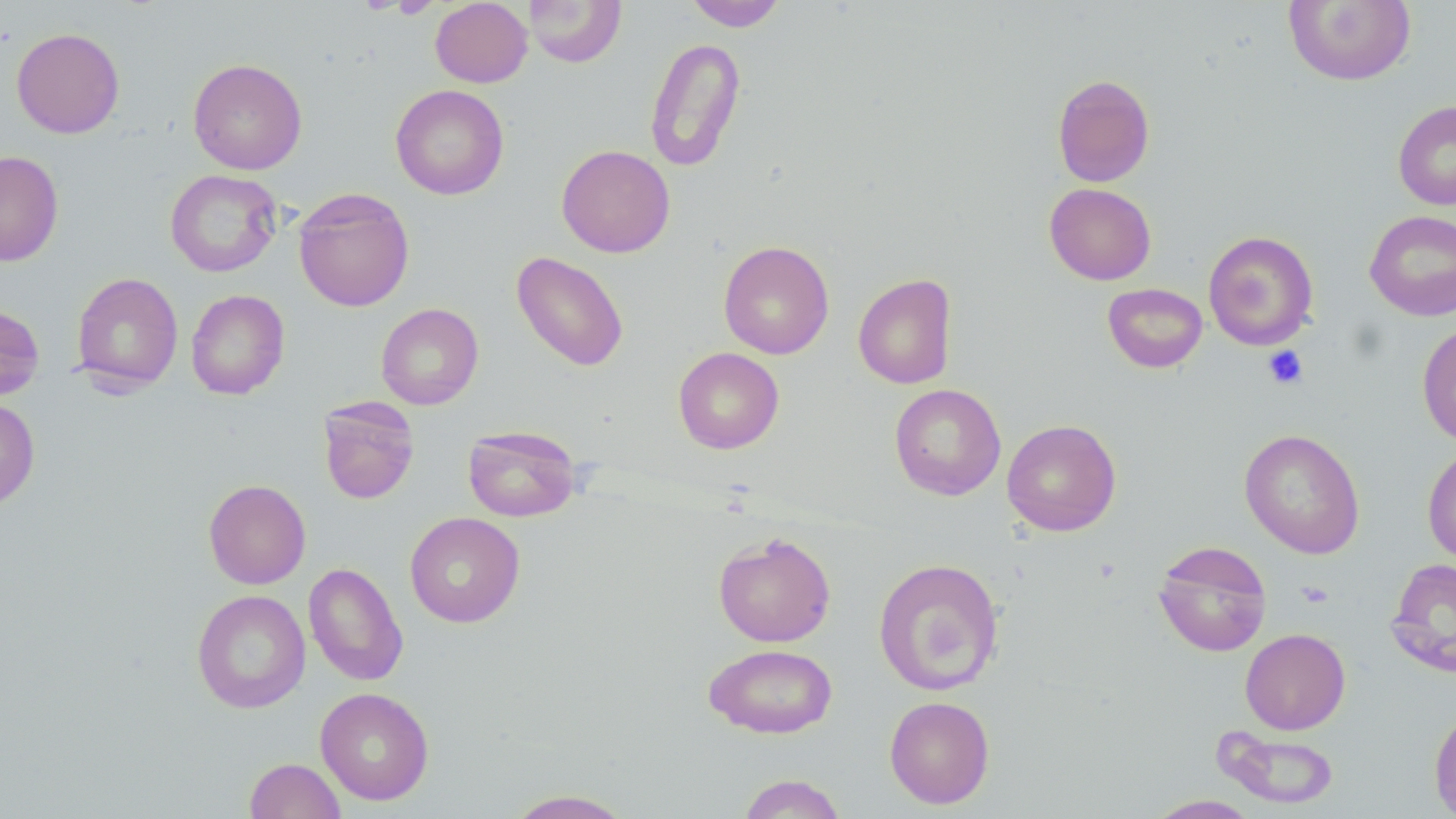
slide-level diagnosis = no evidence of blood parasites
preparation = thin blood smear
field of view = one of a larger specimen
image size = 1456×819 pixels
uninfected red blood cell locations = approximate bounding boxes as [x1, y1, x2, y2] in pixels: [430, 0, 532, 87], [523, 0, 627, 67], [685, 0, 787, 31], [1283, 0, 1416, 86], [11, 28, 124, 138], [644, 36, 746, 172], [188, 58, 307, 175], [1052, 74, 1155, 187], [390, 84, 509, 200], [1392, 100, 1456, 210], [556, 144, 675, 258], [0, 151, 64, 267], [165, 169, 283, 277], [1044, 182, 1156, 285], [293, 188, 414, 312], [1364, 210, 1456, 320], [1203, 230, 1319, 350], [718, 240, 834, 360], [511, 251, 629, 372], [70, 272, 183, 392], [853, 273, 957, 389], [1102, 283, 1208, 373], [185, 289, 290, 400], [376, 303, 483, 410], [0, 304, 45, 401], [1417, 322, 1456, 447], [673, 347, 784, 454], [889, 383, 1006, 500], [317, 397, 420, 504], [0, 398, 40, 510], [1002, 418, 1121, 536], [462, 425, 581, 522], [1239, 428, 1365, 559], [1422, 445, 1456, 564], [203, 479, 311, 589], [404, 511, 526, 628], [713, 532, 836, 647], [1153, 540, 1272, 657], [873, 557, 1004, 695], [1386, 557, 1456, 678], [304, 562, 408, 686], [192, 589, 310, 713], [1240, 628, 1350, 734], [703, 643, 838, 739], [315, 687, 435, 806], [884, 695, 995, 809], [1429, 707, 1456, 817], [1217, 729, 1340, 809], [244, 758, 345, 818], [736, 773, 847, 819], [503, 789, 636, 818], [1146, 795, 1262, 818]
stain = May-Grünwald-Giemsa
platelet locations = approximate bounding boxes as [x1, y1, x2, y2] in pixels: [1263, 346, 1308, 389]
modality = optical microscopy
magnification = 1000x